Give the position of every malaria parasite.
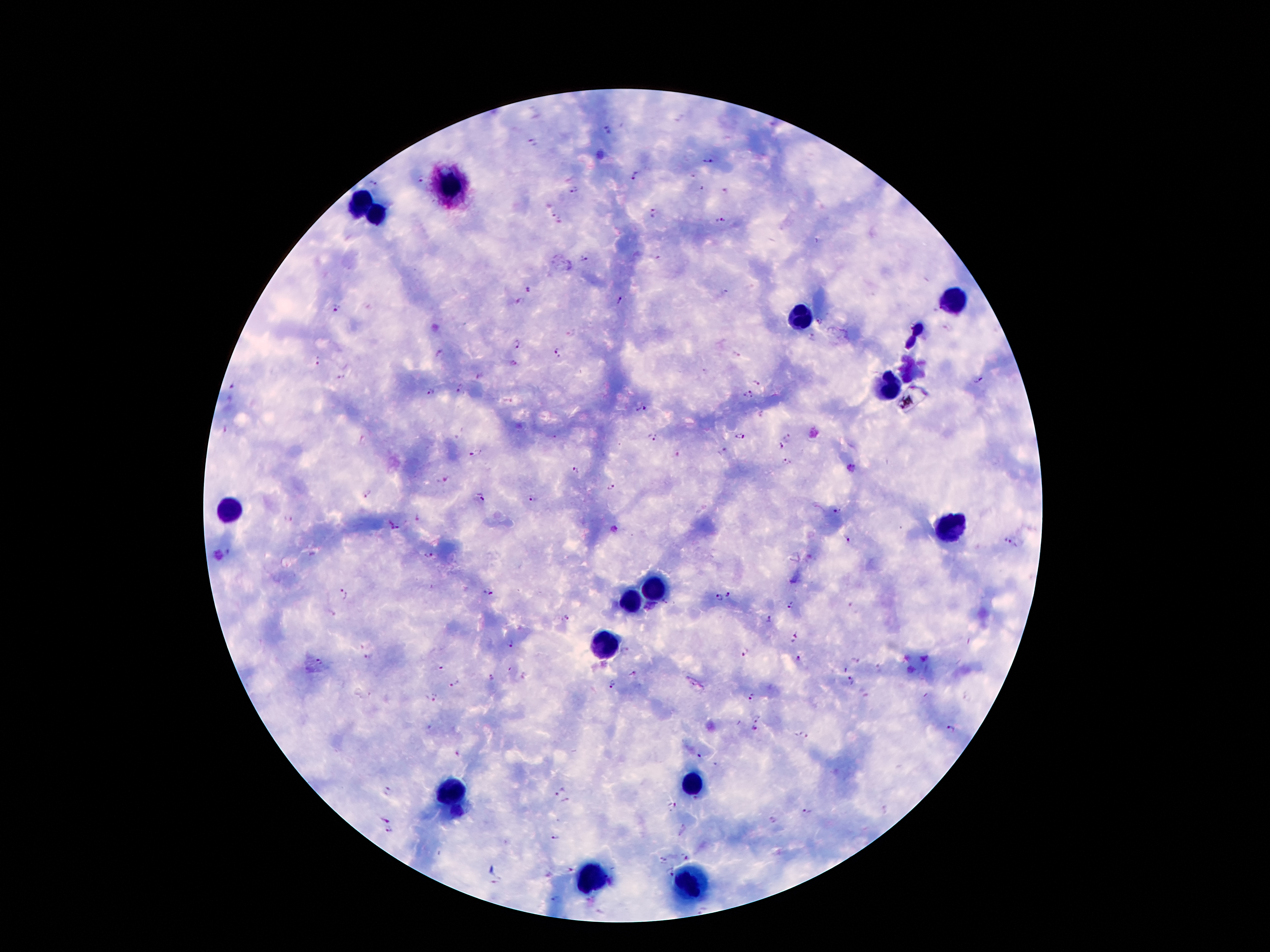
Approximate object centers, in pixels from the top-left corner.
Malaria parasites: (x=609, y=129), (x=534, y=143), (x=708, y=161), (x=635, y=176), (x=419, y=180), (x=372, y=182), (x=700, y=189), (x=573, y=191), (x=724, y=191), (x=652, y=214), (x=555, y=219), (x=720, y=221), (x=584, y=259), (x=530, y=290), (x=724, y=292), (x=519, y=301), (x=619, y=301), (x=338, y=307), (x=811, y=337), (x=516, y=345), (x=438, y=352), (x=557, y=352), (x=737, y=355), (x=318, y=362), (x=513, y=364), (x=479, y=375), (x=342, y=377), (x=979, y=381), (x=757, y=383), (x=233, y=386), (x=458, y=389), (x=430, y=393), (x=746, y=396), (x=641, y=409), (x=226, y=430), (x=738, y=436), (x=554, y=437), (x=652, y=438), (x=789, y=438), (x=781, y=446), (x=724, y=452), (x=475, y=455), (x=787, y=462), (x=575, y=470), (x=446, y=481), (x=611, y=487), (x=367, y=493), (x=480, y=497), (x=532, y=499), (x=836, y=514), (x=289, y=518), (x=417, y=518), (x=394, y=526), (x=847, y=540), (x=1008, y=540), (x=230, y=551), (x=217, y=556), (x=429, y=556), (x=345, y=593), (x=489, y=593), (x=728, y=594), (x=718, y=597), (x=791, y=605), (x=567, y=617), (x=768, y=619), (x=795, y=638), (x=510, y=644), (x=746, y=653), (x=369, y=656), (x=926, y=657), (x=906, y=659), (x=319, y=660), (x=797, y=660), (x=856, y=660), (x=439, y=666), (x=879, y=668), (x=911, y=670), (x=843, y=671), (x=634, y=673), (x=491, y=679), (x=850, y=680), (x=454, y=685), (x=612, y=685), (x=752, y=697), (x=433, y=700), (x=756, y=716), (x=753, y=728), (x=950, y=728), (x=803, y=737), (x=458, y=753), (x=700, y=756), (x=716, y=764), (x=556, y=789), (x=388, y=792), (x=695, y=800), (x=566, y=802), (x=672, y=807), (x=808, y=812), (x=386, y=819), (x=774, y=819), (x=389, y=831), (x=555, y=839), (x=685, y=856), (x=662, y=860), (x=571, y=871), (x=668, y=872), (x=495, y=883), (x=556, y=900).

Summary:
  - Leukocyte locations: (x=451, y=185), (x=364, y=202), (x=376, y=215), (x=955, y=302), (x=801, y=316), (x=917, y=329), (x=909, y=343), (x=910, y=375), (x=889, y=386), (x=232, y=508), (x=957, y=526), (x=650, y=585), (x=634, y=599), (x=609, y=642), (x=693, y=785), (x=450, y=791), (x=591, y=878), (x=691, y=885)
  - Magnification: 100x
  - Preparation: thick peripheral-blood smear
  - Stain: Giemsa
  - Image size: 1270×952 pixels
  - Patient malaria status: infected with Plasmodium falciparum
  - Field of view: one from this slide
  - Capture: smartphone through the microscope eyepiece